Locate every Plasmodium vivax-infected red blood cell.
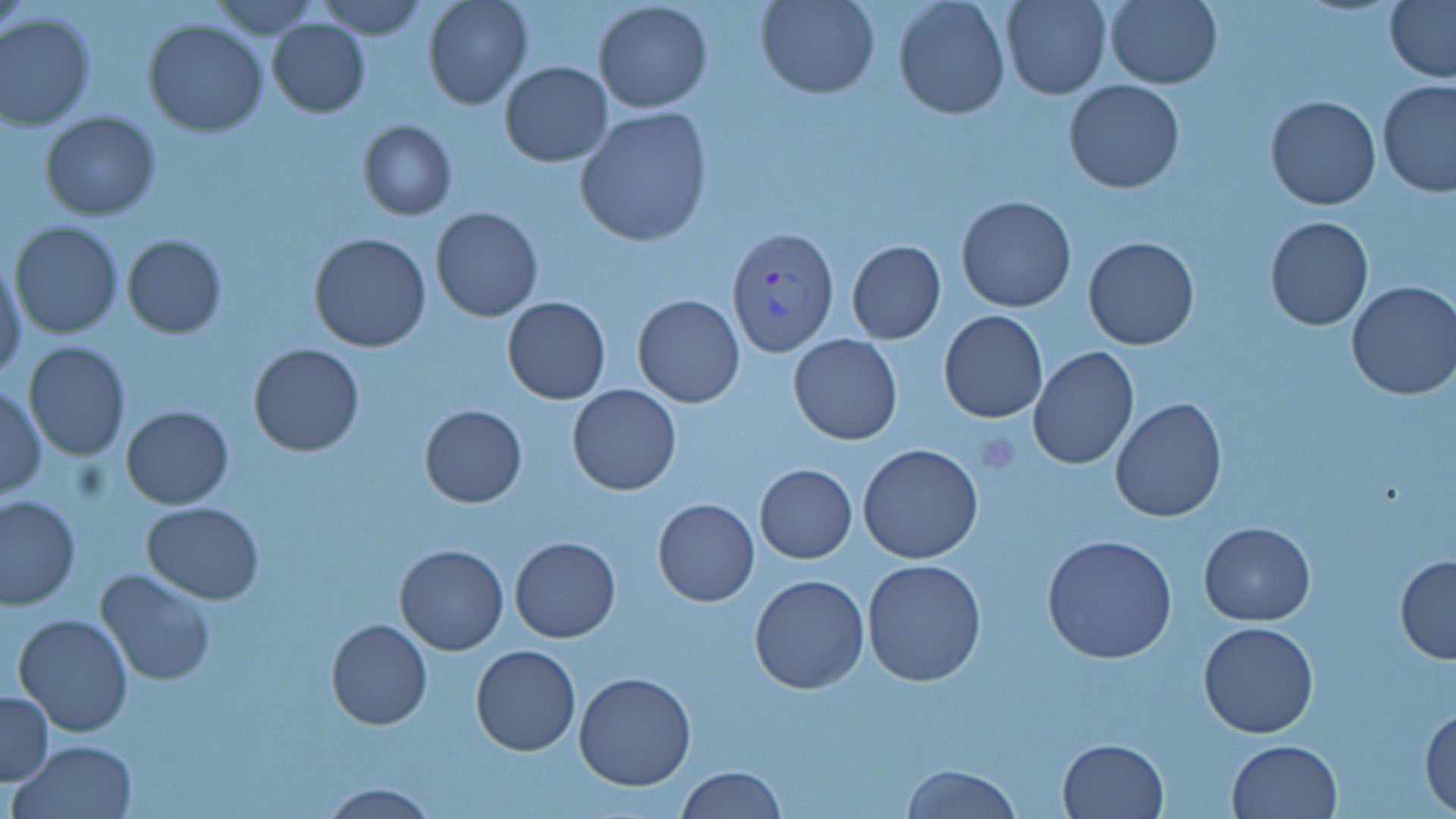

Approximate bounding boxes as named x1/y1/x2/y2 corners in pixels.
Plasmodium vivax-infected red blood cells: (x1=728, y1=227, x2=839, y2=355).

Uninfected red blood cell locations: (x1=207, y1=0, x2=322, y2=39), (x1=319, y1=0, x2=427, y2=38), (x1=425, y1=0, x2=533, y2=109), (x1=757, y1=0, x2=879, y2=98), (x1=893, y1=0, x2=1010, y2=120), (x1=1001, y1=0, x2=1110, y2=99), (x1=1105, y1=0, x2=1222, y2=89), (x1=1385, y1=0, x2=1456, y2=84), (x1=593, y1=1, x2=713, y2=114), (x1=0, y1=12, x2=96, y2=130), (x1=266, y1=18, x2=370, y2=117), (x1=143, y1=19, x2=268, y2=137), (x1=499, y1=62, x2=613, y2=166), (x1=1063, y1=80, x2=1185, y2=194), (x1=1378, y1=80, x2=1456, y2=199), (x1=1265, y1=95, x2=1381, y2=209), (x1=575, y1=108, x2=712, y2=247), (x1=41, y1=110, x2=160, y2=221), (x1=357, y1=120, x2=456, y2=220), (x1=955, y1=196, x2=1076, y2=313), (x1=430, y1=207, x2=542, y2=321), (x1=1264, y1=215, x2=1373, y2=329), (x1=10, y1=221, x2=123, y2=337), (x1=309, y1=233, x2=431, y2=352), (x1=122, y1=235, x2=227, y2=338), (x1=1084, y1=236, x2=1199, y2=350), (x1=847, y1=241, x2=946, y2=344), (x1=1, y1=258, x2=27, y2=382), (x1=1346, y1=281, x2=1456, y2=401), (x1=632, y1=294, x2=744, y2=408), (x1=501, y1=297, x2=611, y2=405), (x1=939, y1=310, x2=1048, y2=423), (x1=788, y1=334, x2=903, y2=444), (x1=22, y1=341, x2=132, y2=461), (x1=249, y1=344, x2=364, y2=457), (x1=1028, y1=346, x2=1140, y2=469), (x1=0, y1=384, x2=47, y2=502), (x1=568, y1=384, x2=681, y2=495), (x1=1110, y1=397, x2=1227, y2=522), (x1=420, y1=404, x2=526, y2=508), (x1=120, y1=406, x2=234, y2=509), (x1=858, y1=444, x2=984, y2=565), (x1=755, y1=464, x2=857, y2=563), (x1=0, y1=494, x2=80, y2=609), (x1=652, y1=499, x2=759, y2=606), (x1=141, y1=500, x2=264, y2=603), (x1=1199, y1=521, x2=1315, y2=625), (x1=1043, y1=533, x2=1178, y2=665), (x1=509, y1=537, x2=621, y2=643), (x1=394, y1=544, x2=508, y2=655), (x1=1394, y1=555, x2=1456, y2=665), (x1=860, y1=559, x2=987, y2=687), (x1=95, y1=567, x2=216, y2=686), (x1=750, y1=574, x2=869, y2=693), (x1=12, y1=612, x2=132, y2=738), (x1=326, y1=619, x2=432, y2=730), (x1=1198, y1=621, x2=1319, y2=739), (x1=470, y1=644, x2=580, y2=755), (x1=573, y1=673, x2=696, y2=791), (x1=0, y1=689, x2=53, y2=786), (x1=1420, y1=704, x2=1456, y2=813), (x1=1057, y1=737, x2=1168, y2=818), (x1=10, y1=739, x2=140, y2=819), (x1=1226, y1=739, x2=1344, y2=819), (x1=900, y1=763, x2=1020, y2=818), (x1=676, y1=765, x2=786, y2=819), (x1=317, y1=781, x2=441, y2=818). Slide-level diagnosis: Plasmodium vivax. May-Grünwald-Giemsa-stained preparation. Thin blood smear. Single field of view. Image is 1456×819 pixels. Light microscopy. 1000x magnification.